Locate every Plasmodium parasite.
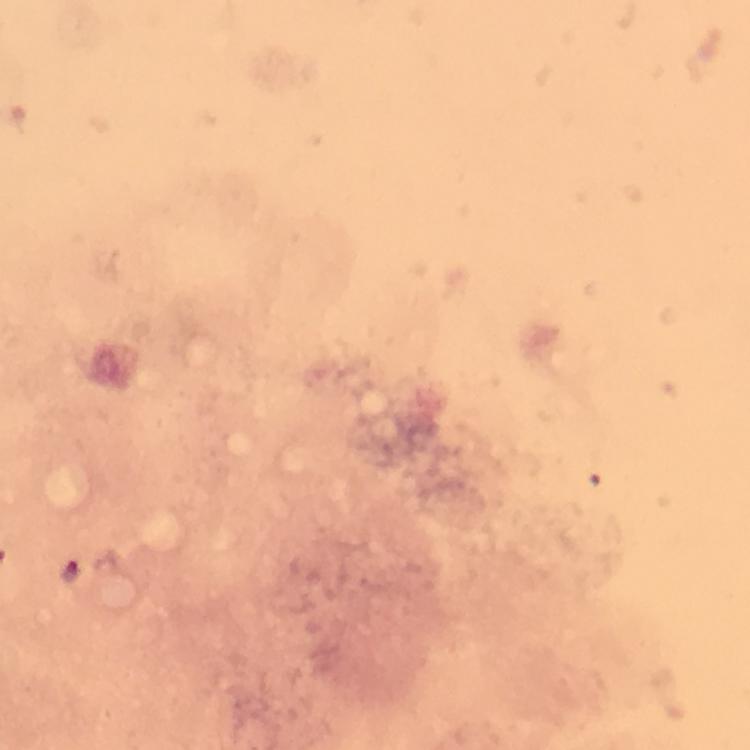
Approximate object centers, in pixels from the top-left corner.
Plasmodium parasites: (x=70, y=571).

Summary:
  - Immersion oil: used
  - Magnification: 100x
  - Stain: Giemsa
  - Image size: 750×750 pixels
  - Capture: smartphone mounted on the microscope
  - Cropped from: a single field of view
  - Context: from a malaria diagnostic workup
  - Preparation: thick blood film